Classify this cell by malaria status.
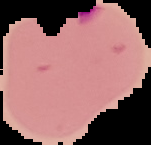

Parasitized.

Image is 151×145 pixels. Segmented cell region on a black background. From a thin blood smear.